State which cell type is depicted.
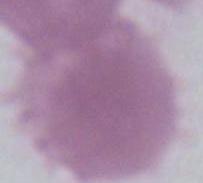

This is an erythrocyte.

Micrograph. 1000x magnification.